Classify this cell by malaria status.
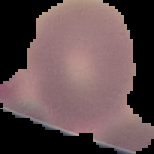

It is uninfected.

{
  "image_size": "154×154 pixels",
  "preparation": "thin blood smear",
  "image_type": "segmented cell region with the area outside set to black"
}